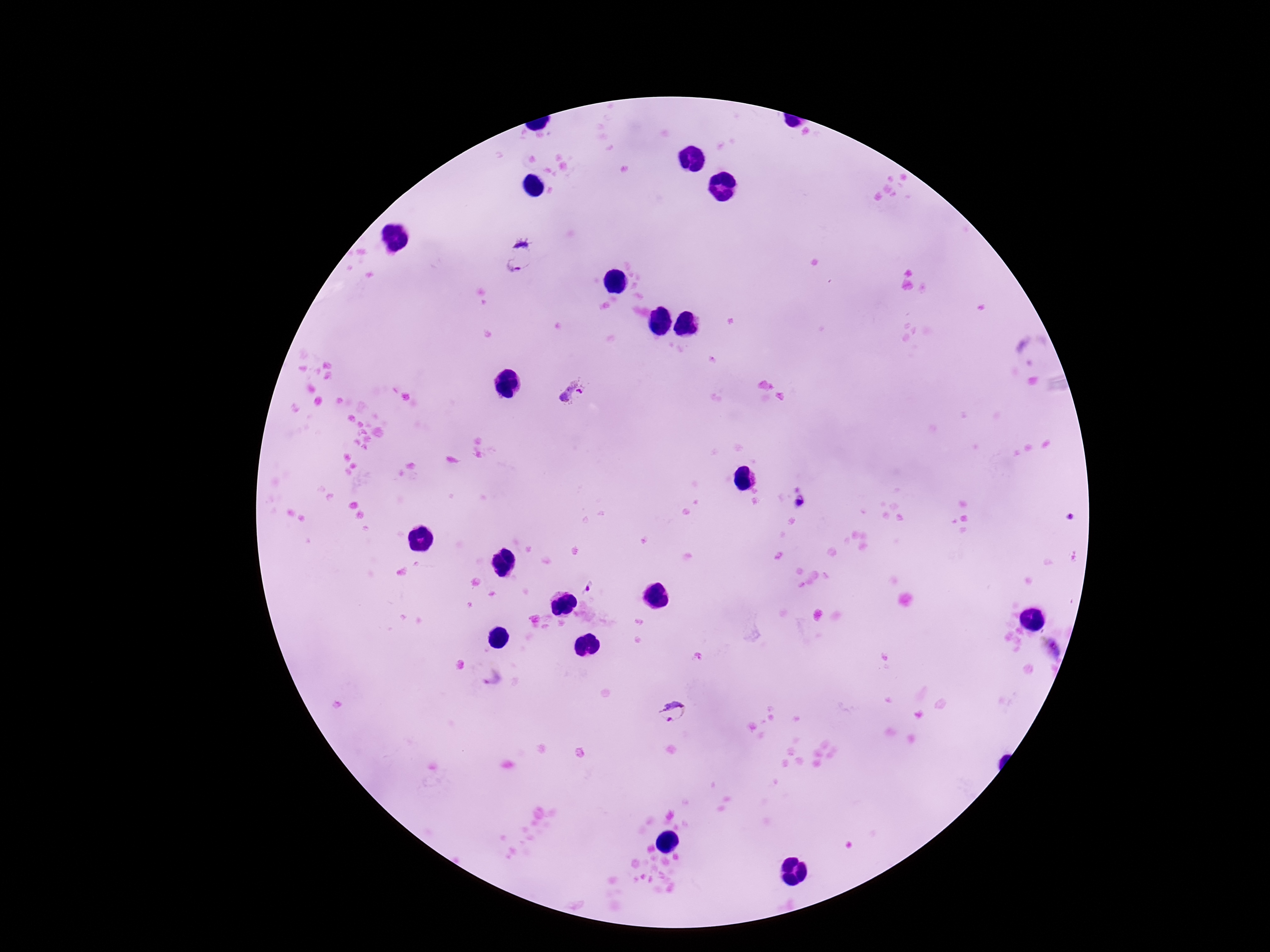
Approximate centers as [x, y] in pixels.
Summary:
  - Plasmodium parasite locations: [516, 257], [1031, 352], [575, 397], [587, 588], [1052, 648], [490, 676], [673, 712]
  - Capture: smartphone camera through the microscope eyepiece
  - Magnification: 100x
  - Patient malaria status: infected
  - Preparation: thick peripheral-blood smear
  - Image size: 1270×952 pixels
  - Stain: Giemsa
  - Field of view: one from this slide